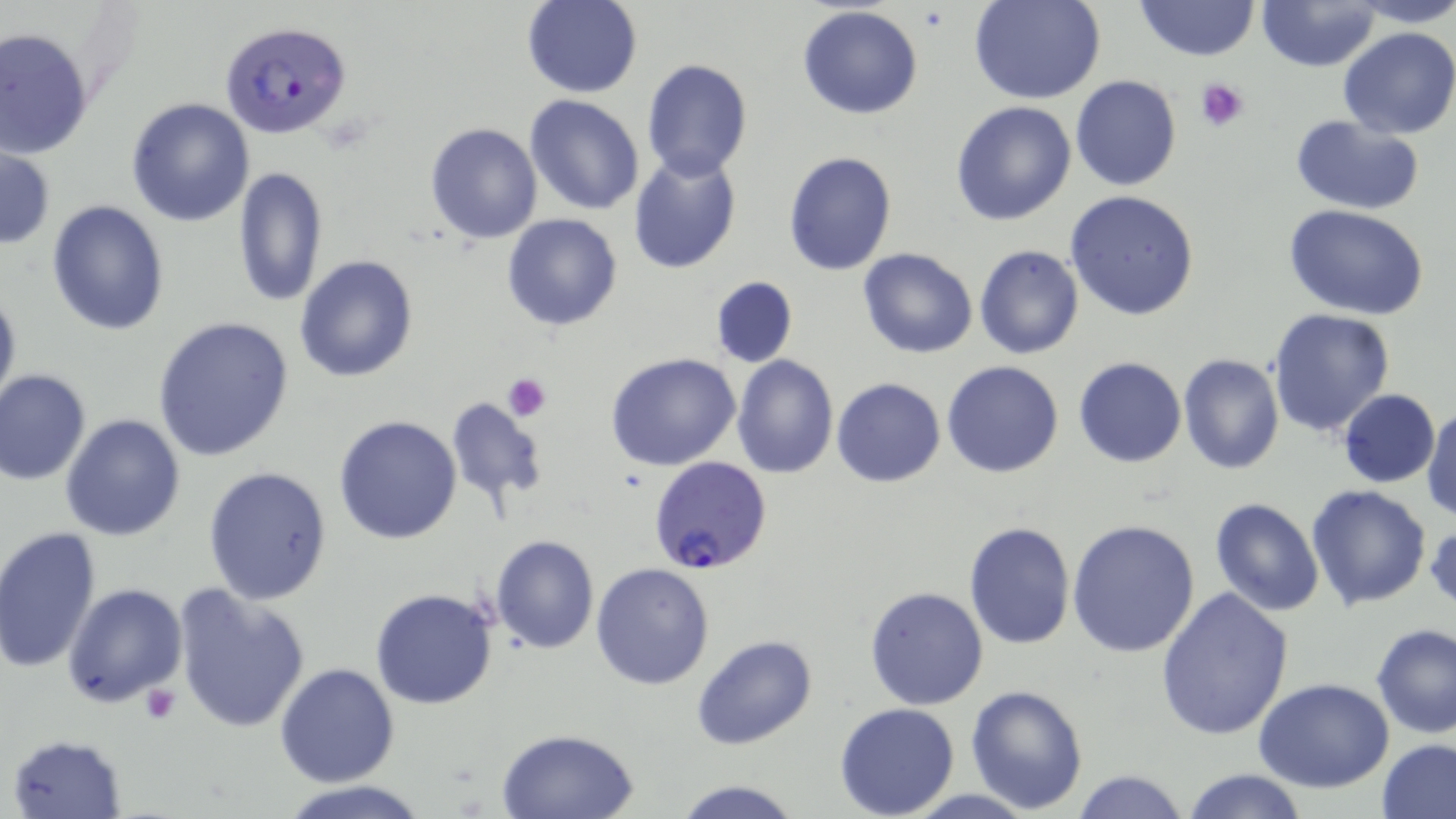

Summary:
  - Coordinate format: approximate bounding boxes as named x1/y1/x2/y2 corners in pixels
  - Plasmodium falciparum-infected red blood cell locations: (x1=219, y1=20, x2=353, y2=140), (x1=649, y1=456, x2=772, y2=575)
  - Platelet locations: (x1=1197, y1=78, x2=1250, y2=131), (x1=502, y1=372, x2=551, y2=419), (x1=140, y1=683, x2=180, y2=724)
  - Uninfected red blood cell locations: (x1=1134, y1=0, x2=1258, y2=62), (x1=1350, y1=0, x2=1456, y2=27), (x1=521, y1=1, x2=642, y2=97), (x1=971, y1=1, x2=1106, y2=105), (x1=1258, y1=1, x2=1380, y2=71), (x1=797, y1=6, x2=923, y2=120), (x1=0, y1=26, x2=94, y2=159), (x1=1338, y1=26, x2=1456, y2=140), (x1=641, y1=60, x2=752, y2=182), (x1=1070, y1=75, x2=1181, y2=192), (x1=524, y1=93, x2=648, y2=215), (x1=125, y1=96, x2=255, y2=226), (x1=950, y1=101, x2=1078, y2=226), (x1=1289, y1=115, x2=1427, y2=215), (x1=426, y1=123, x2=542, y2=243), (x1=1, y1=145, x2=54, y2=250), (x1=784, y1=150, x2=897, y2=277), (x1=627, y1=152, x2=742, y2=275), (x1=231, y1=167, x2=328, y2=308), (x1=1066, y1=191, x2=1201, y2=321), (x1=46, y1=200, x2=170, y2=336), (x1=1284, y1=203, x2=1430, y2=318), (x1=502, y1=213, x2=624, y2=331), (x1=974, y1=246, x2=1084, y2=361), (x1=858, y1=248, x2=979, y2=359), (x1=295, y1=255, x2=419, y2=383), (x1=710, y1=276, x2=798, y2=369), (x1=0, y1=281, x2=21, y2=420), (x1=1266, y1=307, x2=1396, y2=437), (x1=151, y1=315, x2=297, y2=462), (x1=605, y1=352, x2=741, y2=470), (x1=732, y1=354, x2=839, y2=477), (x1=1177, y1=354, x2=1285, y2=476), (x1=1072, y1=356, x2=1186, y2=467), (x1=942, y1=360, x2=1065, y2=478), (x1=0, y1=368, x2=92, y2=485), (x1=832, y1=377, x2=947, y2=487), (x1=1338, y1=389, x2=1440, y2=487), (x1=444, y1=396, x2=549, y2=509), (x1=1422, y1=403, x2=1455, y2=522), (x1=59, y1=414, x2=186, y2=540), (x1=332, y1=415, x2=463, y2=544), (x1=203, y1=465, x2=333, y2=605), (x1=1306, y1=483, x2=1433, y2=610), (x1=1209, y1=498, x2=1325, y2=618), (x1=1427, y1=517, x2=1455, y2=614), (x1=1067, y1=518, x2=1201, y2=657), (x1=964, y1=520, x2=1075, y2=651), (x1=0, y1=525, x2=103, y2=674), (x1=491, y1=535, x2=598, y2=654), (x1=591, y1=562, x2=715, y2=690), (x1=63, y1=583, x2=188, y2=708), (x1=170, y1=583, x2=313, y2=732), (x1=1156, y1=585, x2=1295, y2=740), (x1=865, y1=586, x2=989, y2=710), (x1=369, y1=588, x2=498, y2=709), (x1=1371, y1=622, x2=1456, y2=738), (x1=692, y1=636, x2=817, y2=751), (x1=275, y1=663, x2=399, y2=786), (x1=1254, y1=678, x2=1395, y2=792), (x1=965, y1=684, x2=1090, y2=814), (x1=833, y1=702, x2=961, y2=818), (x1=495, y1=728, x2=640, y2=817), (x1=8, y1=733, x2=127, y2=818), (x1=1377, y1=738, x2=1456, y2=819), (x1=1071, y1=768, x2=1191, y2=819), (x1=1179, y1=768, x2=1311, y2=819), (x1=673, y1=779, x2=801, y2=818), (x1=281, y1=781, x2=429, y2=819)
  - Slide-level diagnosis: Plasmodium falciparum
  - Magnification: 1000x
  - Modality: optical microscopy
  - Image size: 1456×819 pixels
  - Preparation: thin blood smear
  - Stain: May-Grünwald-Giemsa
  - Field of view: single